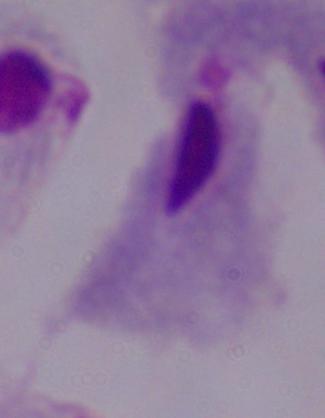
identification = trichomonad
magnification = 1000x
modality = micrograph